State which parasite is depicted.
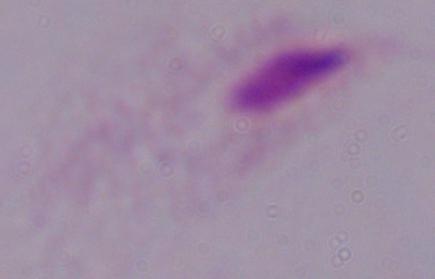
A trichomonad.

Photomicrograph. Captured at 1000x magnification.